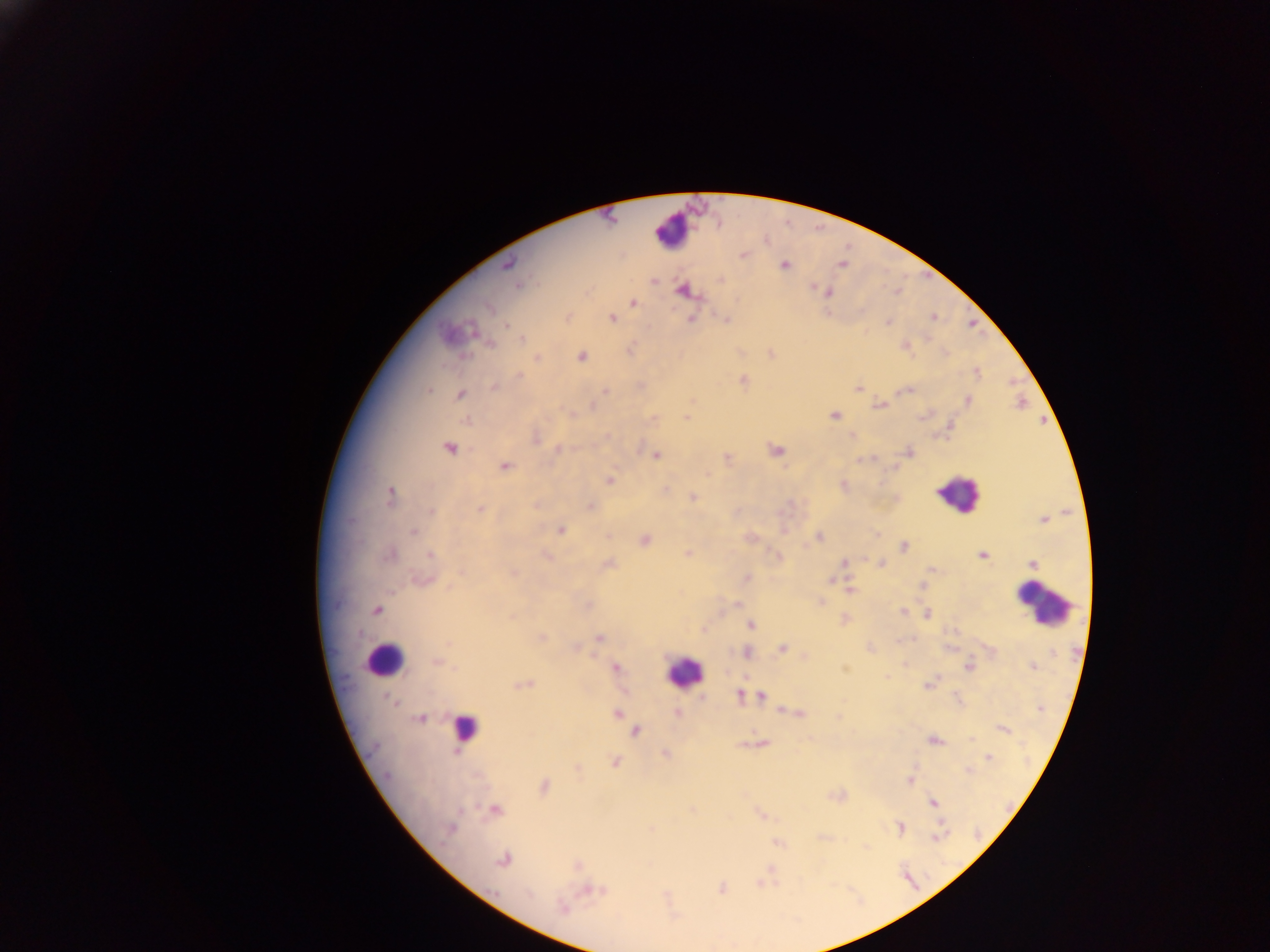

preparation: thick blood smear
field_of_view: single
leukocyte_locations: 'approximate centers as [x, y] in pixels: [674, 231], [957, 493], [1044, 605], [383, 660], [682, 671], [465, 727]'
country: Ghana
plasmodium_parasite_locations: 'approximate centers as [x, y] in pixels: [743, 254], [508, 264], [841, 264], [784, 265], [519, 285], [814, 288], [683, 291], [828, 293], [634, 303], [932, 317], [613, 318], [691, 319], [888, 322], [507, 325], [522, 340], [582, 356], [538, 357], [519, 375], [743, 380], [493, 387], [858, 388], [429, 390], [606, 390], [908, 390], [460, 394], [968, 401], [880, 405], [573, 414], [834, 415], [687, 417], [465, 419], [607, 436], [536, 439], [448, 448], [557, 450], [777, 451], [909, 452], [656, 455], [727, 458], [504, 466], [609, 480], [843, 485], [665, 490], [390, 496], [693, 497], [590, 506], [479, 509], [432, 511], [560, 530], [413, 531], [819, 538], [645, 540], [903, 547], [687, 553], [390, 554], [431, 555], [546, 556], [778, 556], [982, 556], [845, 562], [1033, 563], [609, 564], [882, 564], [932, 569], [460, 573], [513, 573], [747, 578], [422, 580], [831, 580], [922, 586], [850, 590], [821, 602], [738, 603], [589, 605], [376, 610], [903, 612], [927, 615], [511, 617], [750, 625], [541, 637], [600, 638], [448, 642], [782, 648], [576, 649], [748, 653], [436, 663], [969, 666], [1033, 666], [455, 668], [615, 668], [886, 677], [524, 684], [928, 684], [739, 694], [762, 696], [702, 697], [390, 700], [394, 704], [677, 713], [798, 713], [617, 714], [420, 719], [1004, 730], [636, 732], [971, 739], [934, 741], [763, 743], [665, 753], [988, 758], [615, 762], [969, 770], [387, 775], [909, 780], [544, 786], [933, 802], [693, 809], [495, 810], [449, 828], [900, 829], [936, 837], [777, 842], [503, 861], [577, 865], [721, 888], [593, 891], [528, 894], [563, 909]'
capture: mobile-phone photograph through a microscope
image_size: 1270×952 pixels